Name the blood parasite species.
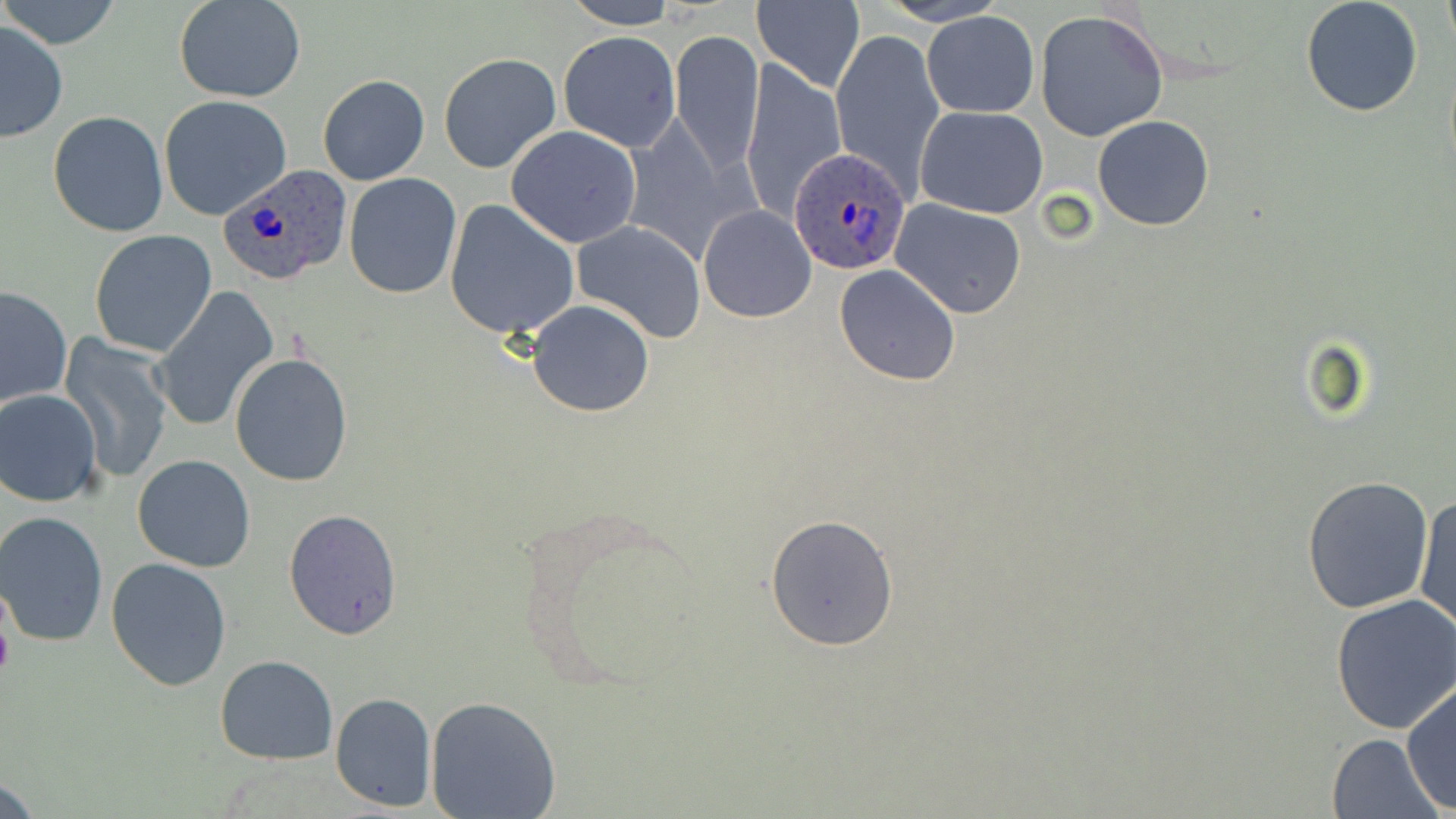
Plasmodium ovale.

Approximate bounding boxes as (x1, y1, x2, y2) in pixels. Uninfected red blood cell locations: (1, 0, 123, 51), (174, 0, 308, 102), (875, 0, 1009, 26), (1301, 0, 1425, 118), (1439, 0, 1454, 55), (561, 1, 679, 29), (752, 1, 865, 93), (1034, 8, 1168, 140), (923, 11, 1039, 118), (0, 21, 69, 141), (830, 28, 945, 199), (669, 29, 765, 180), (557, 30, 682, 151), (437, 52, 561, 173), (738, 59, 848, 223), (317, 73, 429, 186), (158, 95, 293, 222), (916, 105, 1048, 219), (48, 110, 168, 238), (1092, 115, 1214, 233), (504, 125, 642, 247), (344, 172, 462, 298), (889, 199, 1027, 319), (443, 200, 581, 340), (698, 204, 818, 323), (573, 220, 707, 343), (88, 229, 218, 358), (833, 265, 961, 387), (148, 285, 280, 434), (0, 286, 73, 409), (527, 300, 655, 418), (59, 333, 175, 485), (228, 352, 353, 487), (0, 389, 103, 506), (132, 454, 255, 571), (1302, 474, 1436, 615), (1414, 491, 1454, 636), (514, 501, 712, 696), (286, 506, 401, 641), (1, 512, 113, 648), (764, 514, 900, 652), (105, 555, 232, 692), (1330, 593, 1456, 734), (215, 654, 339, 764), (1401, 681, 1456, 812), (330, 692, 437, 812), (425, 696, 562, 818), (1325, 732, 1444, 819). Plasmodium ovale-infected red blood cell locations: (790, 148, 911, 276), (216, 160, 353, 287). May-Grünwald-Giemsa-stained preparation. Image is 1456×819 pixels. Thin blood smear. Optical microscopy. Single field of view. Captured at 1000x magnification.